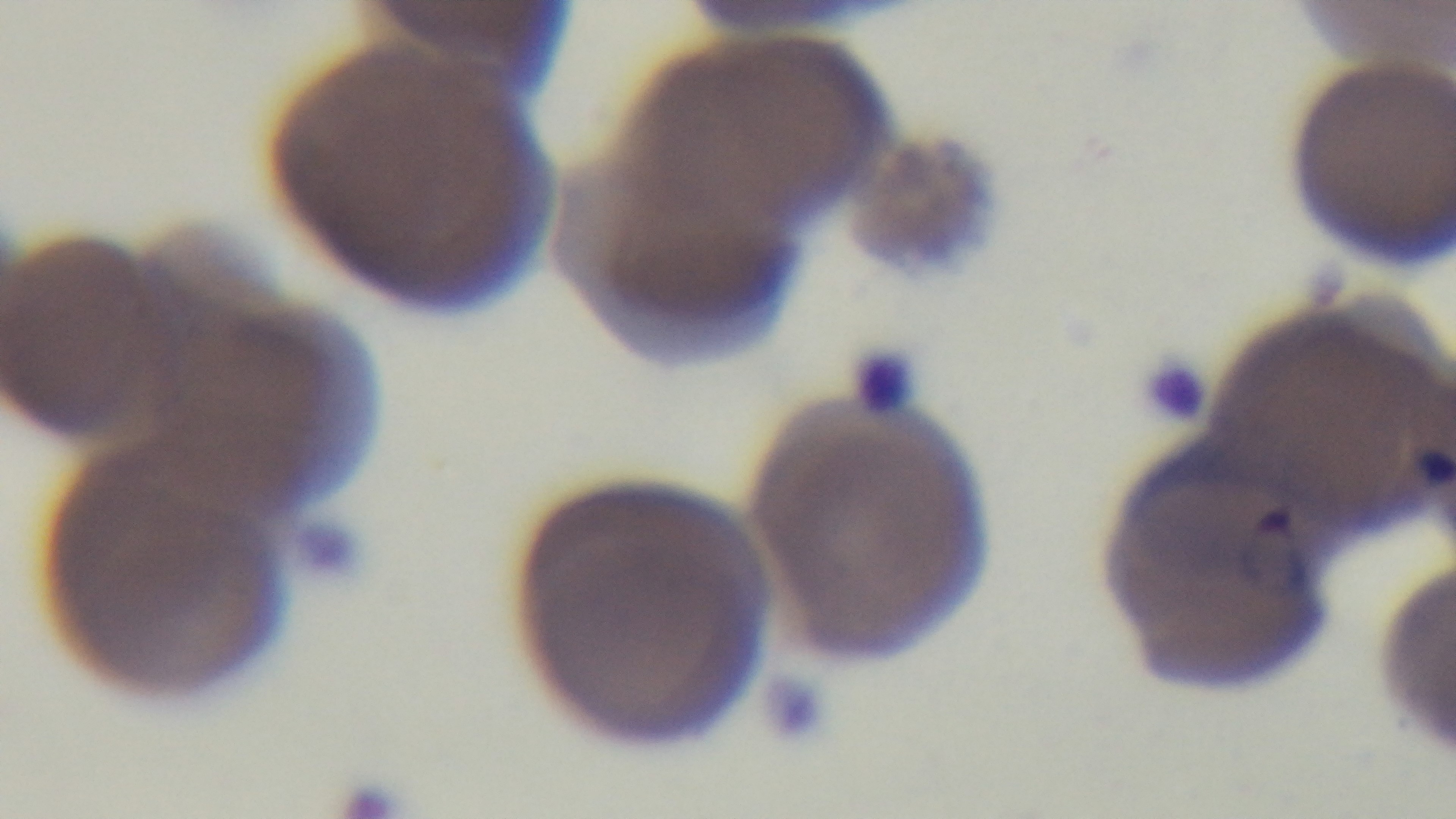

Summary:
  - Malaria status: positive
  - Stain: Giemsa
  - Objective: 100x oil immersion
  - Preparation: thin
  - Field of view: single
  - Capture: mounted 4K digital camera
  - Modality: light microscopy